Identify the preparation type.
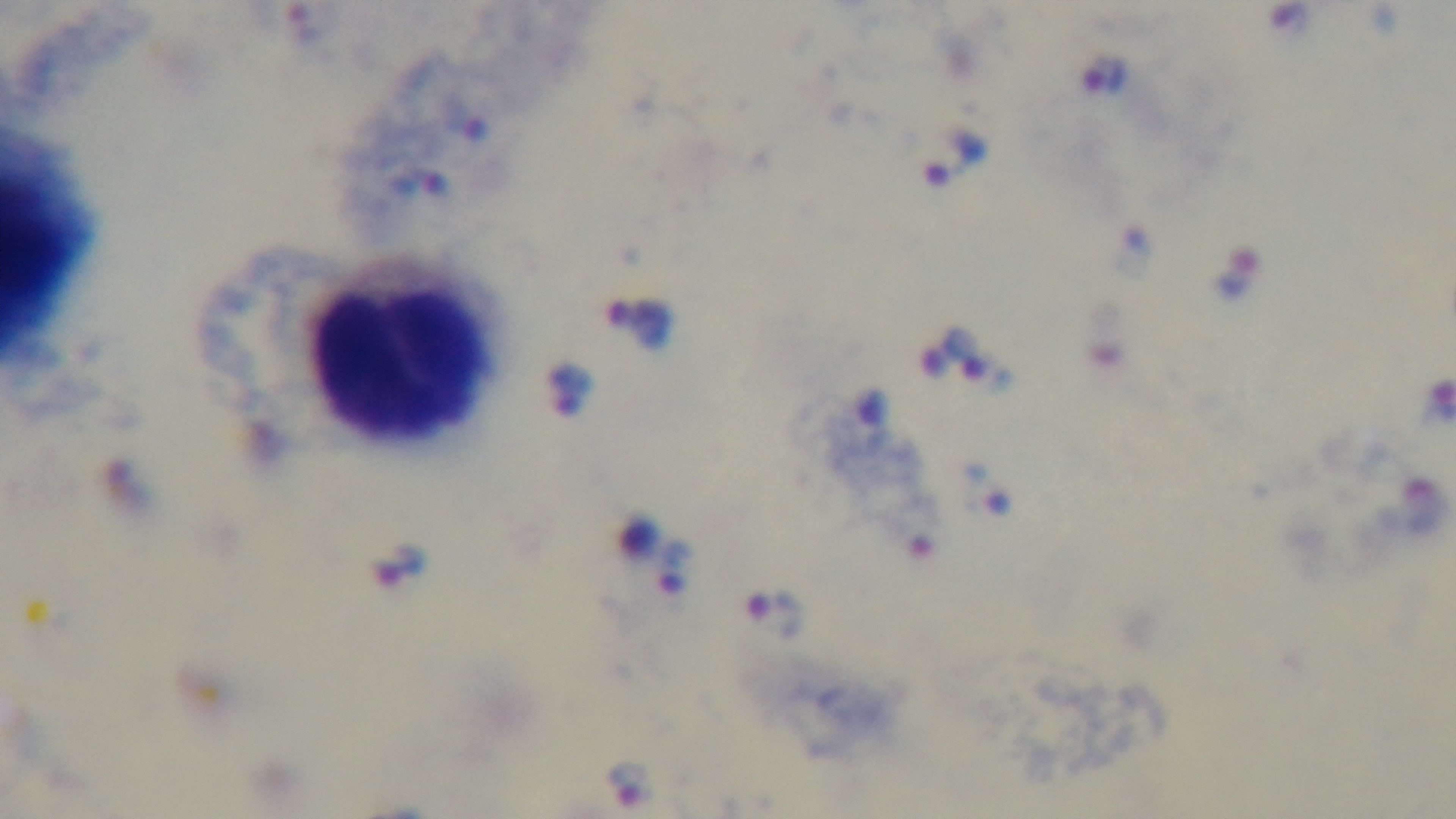

Thick.

Summary:
  - Malaria status: infected
  - Field of view: single
  - Objective: 100x oil immersion
  - Modality: light microscopy
  - Capture: mounted 4K digital camera
  - Stain: Giemsa